State which parasite is depicted.
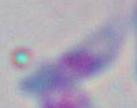
This is Toxoplasma gondii.

{
  "magnification": "1000x",
  "modality": "micrograph"
}